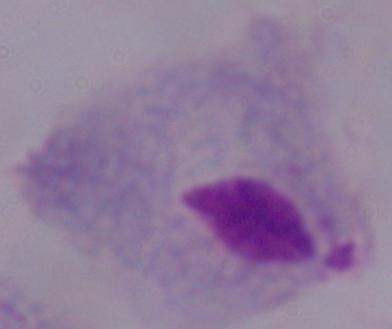

A trichomonad is shown. 1000x magnification. Photomicrograph.